Mark where platelets are.
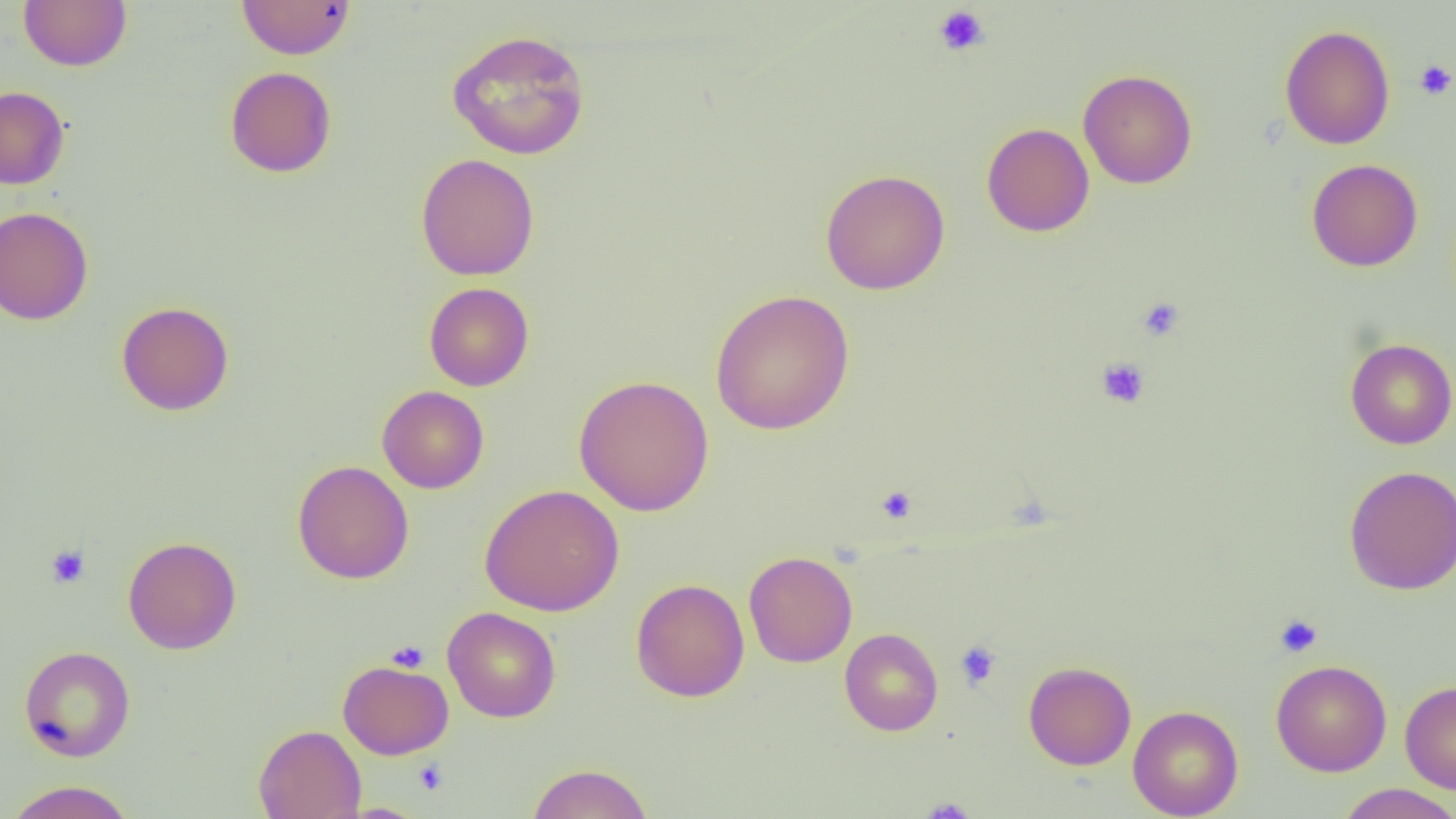
Approximate bounding boxes as named x1/y1/x2/y2 corners in pixels.
Platelets: (x1=933, y1=5, x2=991, y2=57), (x1=1414, y1=59, x2=1456, y2=100), (x1=1137, y1=297, x2=1184, y2=341), (x1=1096, y1=357, x2=1149, y2=408), (x1=876, y1=485, x2=917, y2=524), (x1=46, y1=544, x2=91, y2=587), (x1=1275, y1=614, x2=1323, y2=658), (x1=386, y1=640, x2=429, y2=672), (x1=955, y1=640, x2=1002, y2=690), (x1=413, y1=760, x2=449, y2=796), (x1=919, y1=798, x2=976, y2=818).

Summary:
  - Uninfected red blood cell locations: (x1=19, y1=0, x2=132, y2=71), (x1=237, y1=0, x2=356, y2=59), (x1=1279, y1=24, x2=1395, y2=150), (x1=446, y1=28, x2=591, y2=160), (x1=225, y1=66, x2=337, y2=178), (x1=1078, y1=69, x2=1197, y2=189), (x1=0, y1=86, x2=70, y2=189), (x1=981, y1=122, x2=1095, y2=237), (x1=415, y1=153, x2=540, y2=281), (x1=1306, y1=158, x2=1423, y2=272), (x1=820, y1=168, x2=950, y2=295), (x1=0, y1=206, x2=94, y2=325), (x1=424, y1=282, x2=534, y2=391), (x1=710, y1=289, x2=854, y2=435), (x1=116, y1=301, x2=234, y2=415), (x1=1345, y1=338, x2=1456, y2=449), (x1=574, y1=374, x2=714, y2=517), (x1=377, y1=385, x2=489, y2=493), (x1=292, y1=460, x2=414, y2=584), (x1=1343, y1=464, x2=1456, y2=595), (x1=479, y1=484, x2=624, y2=616), (x1=122, y1=536, x2=241, y2=654), (x1=743, y1=550, x2=858, y2=667), (x1=631, y1=578, x2=749, y2=702), (x1=442, y1=606, x2=561, y2=722), (x1=839, y1=628, x2=943, y2=736), (x1=19, y1=645, x2=136, y2=761), (x1=337, y1=659, x2=454, y2=759), (x1=1023, y1=660, x2=1137, y2=770), (x1=1271, y1=660, x2=1392, y2=777), (x1=1400, y1=679, x2=1456, y2=794), (x1=1127, y1=704, x2=1244, y2=818), (x1=253, y1=724, x2=366, y2=819), (x1=525, y1=763, x2=654, y2=819), (x1=3, y1=780, x2=138, y2=819), (x1=1335, y1=784, x2=1455, y2=819)
  - Slide-level diagnosis: negative for blood parasites
  - Field of view: single
  - Magnification: 1000x
  - Modality: light microscopy
  - Preparation: thin blood film
  - Image size: 1456×819 pixels